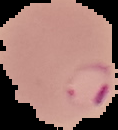
{
  "result": "malaria parasites detected",
  "image_size": "118×130 pixels",
  "image_type": "cell region segmented out of the field of view; surrounding area masked to black",
  "preparation": "thin blood film"
}